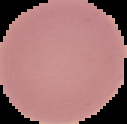
result = no Plasmodium parasites seen
preparation = thin blood smear
image size = 127×124 pixels
image type = segmented cell region with the area outside set to black